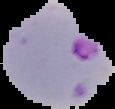

image_size: 115×109 pixels
result: malaria parasites identified
preparation: thin blood film
image_type: segmented cell region with the area outside set to black